Report the malaria status of this cell.
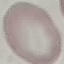

It is uninfected.

Summary:
  - Preparation: thin smear
  - Capture: smartphone camera at the microscope eyepiece
  - Image type: automatically extracted cell patch, resized to 64 × 64 pixels
  - Stain: Giemsa